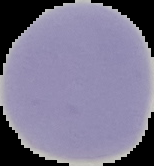

preparation: thin blood smear
image_size: 154×166 pixels
malaria_status: uninfected
image_type: cell region segmented out of the field of view; surrounding area masked to black